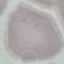

Malaria status: uninfected. Thin blood smear. Cell patch, automatically extracted from a larger field of view and resized to 64 × 64 pixels. Photographed with a smartphone camera at the microscope eyepiece. Giemsa stain.